Assess this cell for malaria.
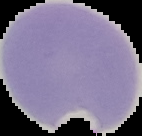
It is parasitized.

From a thin blood smear. Image is 142×136 pixels. Cell region segmented out of the field of view; the surrounding area is masked to black.